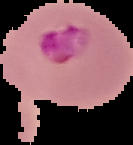

Summary:
  - Malaria status: parasitized
  - Image size: 133×145 pixels
  - Preparation: thin blood smear
  - Image type: segmented cell region on a black background